Locate every blood parasite and identify its species.
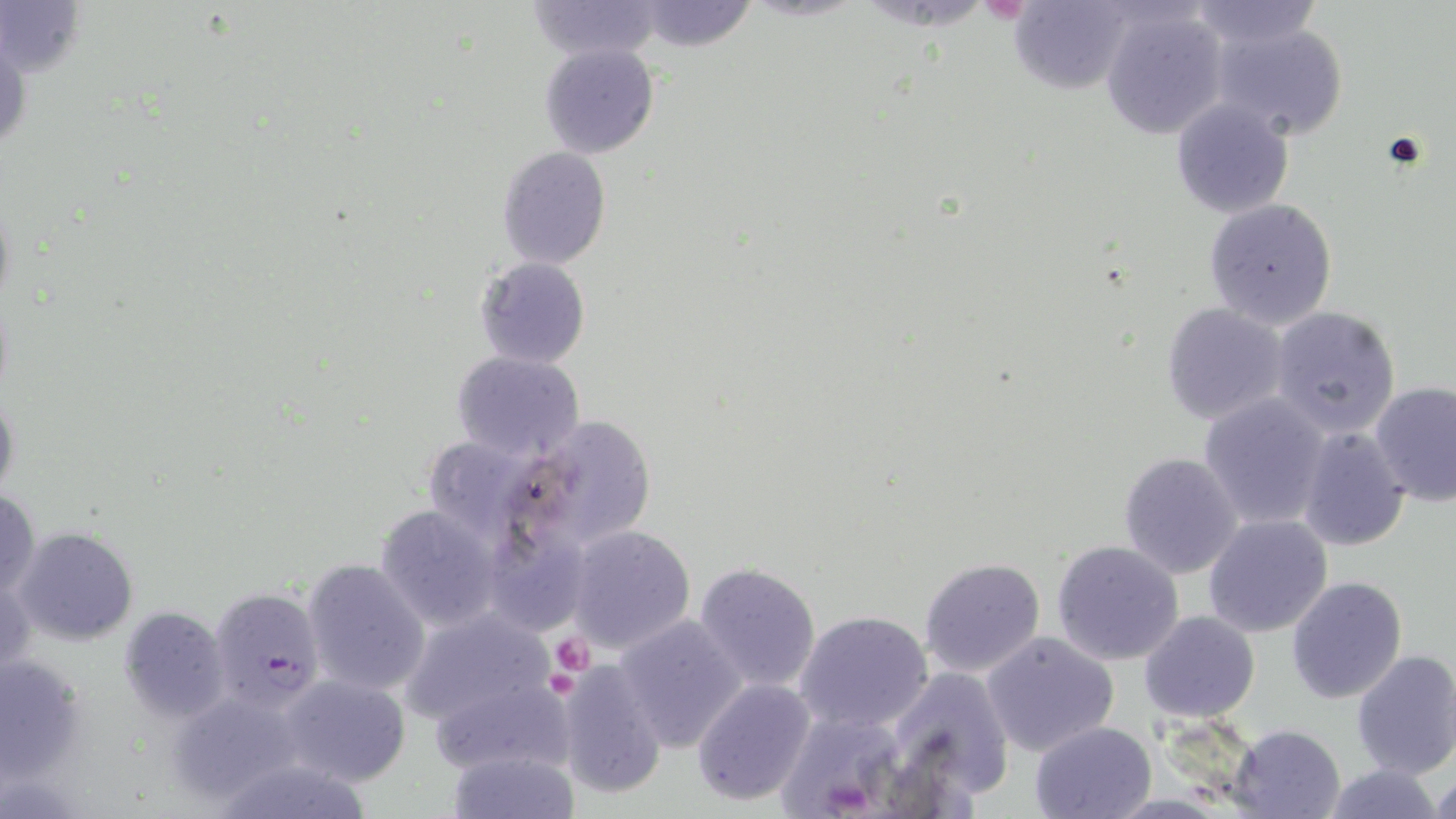

Approximate bounding boxes as named x1/y1/x2/y2 corners in pixels.
Plasmodium falciparum-infected red blood cells: (x1=210, y1=585, x2=327, y2=712).
No Plasmodium ovale, Plasmodium malariae, Plasmodium vivax, Babesia divergens, or Trypanosoma brucei observed.

Summary:
  - Platelet locations: (x1=548, y1=632, x2=595, y2=676)
  - Uninfected red blood cell locations: (x1=525, y1=0, x2=664, y2=62), (x1=1182, y1=0, x2=1322, y2=47), (x1=632, y1=1, x2=757, y2=52), (x1=1, y1=2, x2=86, y2=80), (x1=1009, y1=3, x2=1133, y2=96), (x1=1098, y1=4, x2=1229, y2=139), (x1=1207, y1=17, x2=1350, y2=142), (x1=540, y1=43, x2=659, y2=159), (x1=1171, y1=99, x2=1295, y2=218), (x1=497, y1=147, x2=611, y2=268), (x1=1202, y1=197, x2=1338, y2=328), (x1=475, y1=257, x2=590, y2=369), (x1=1159, y1=302, x2=1291, y2=426), (x1=1268, y1=305, x2=1402, y2=438), (x1=450, y1=349, x2=585, y2=462), (x1=1369, y1=380, x2=1456, y2=503), (x1=0, y1=386, x2=20, y2=504), (x1=1198, y1=394, x2=1332, y2=530), (x1=513, y1=415, x2=658, y2=553), (x1=1296, y1=426, x2=1411, y2=552), (x1=418, y1=435, x2=545, y2=548), (x1=1118, y1=453, x2=1244, y2=579), (x1=0, y1=486, x2=40, y2=603), (x1=375, y1=504, x2=503, y2=632), (x1=1203, y1=515, x2=1333, y2=638), (x1=563, y1=525, x2=696, y2=654), (x1=15, y1=527, x2=138, y2=645), (x1=1051, y1=540, x2=1184, y2=665), (x1=919, y1=556, x2=1047, y2=678), (x1=301, y1=558, x2=432, y2=696), (x1=692, y1=560, x2=821, y2=693), (x1=1286, y1=575, x2=1407, y2=704), (x1=119, y1=605, x2=231, y2=723), (x1=400, y1=608, x2=559, y2=731), (x1=795, y1=611, x2=931, y2=733), (x1=1139, y1=611, x2=1261, y2=722), (x1=611, y1=613, x2=750, y2=753), (x1=980, y1=631, x2=1120, y2=757), (x1=1352, y1=649, x2=1456, y2=780), (x1=0, y1=651, x2=87, y2=786), (x1=551, y1=660, x2=665, y2=800), (x1=889, y1=664, x2=1015, y2=798), (x1=427, y1=672, x2=574, y2=775), (x1=280, y1=674, x2=412, y2=787), (x1=692, y1=678, x2=816, y2=806), (x1=168, y1=687, x2=309, y2=805), (x1=777, y1=711, x2=909, y2=819), (x1=1029, y1=721, x2=1157, y2=819), (x1=1229, y1=724, x2=1345, y2=819), (x1=446, y1=748, x2=581, y2=819), (x1=1319, y1=763, x2=1447, y2=819), (x1=1430, y1=770, x2=1456, y2=819)
  - Slide-level diagnosis: Plasmodium falciparum
  - Preparation: thin blood smear
  - Stain: May-Grünwald-Giemsa
  - Field of view: one of a larger specimen
  - Magnification: 1000x
  - Modality: light microscopy
  - Image size: 1456×819 pixels